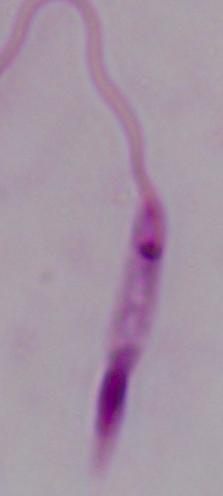

Summary:
  - Magnification: 1000x
  - Modality: micrograph
  - Identification: Leishmania